Point out each malaria parasite.
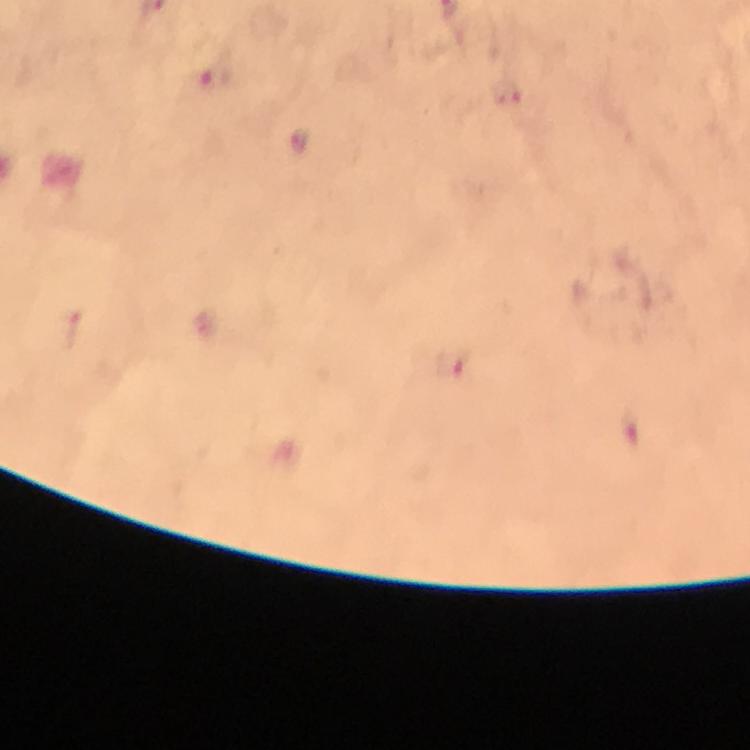

Approximate object centers, in pixels from the top-left corner.
Malaria parasites: (x=216, y=77), (x=508, y=93), (x=299, y=141), (x=452, y=365).

Summary:
  - Context: from a malaria diagnostic workup
  - Magnification: 100x
  - Cropped from: one field of view
  - Stain: Giemsa
  - Image size: 750×750 pixels
  - Immersion oil: applied
  - Capture: smartphone photograph through a microscope
  - Preparation: thick smear